Report the malaria status of this cell.
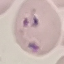
Parasitized.

Summary:
  - Capture: smartphone camera at the microscope eyepiece
  - Stain: Giemsa
  - Preparation: thin smear
  - Image type: automatically extracted cell patch, resized to 64 × 64 pixels